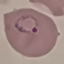

Summary:
  - Result: malaria parasites identified
  - Preparation: thin blood smear
  - Image type: automatically extracted cell patch, resized to 64 × 64 pixels
  - Stain: Giemsa
  - Capture: smartphone through the microscope eyepiece